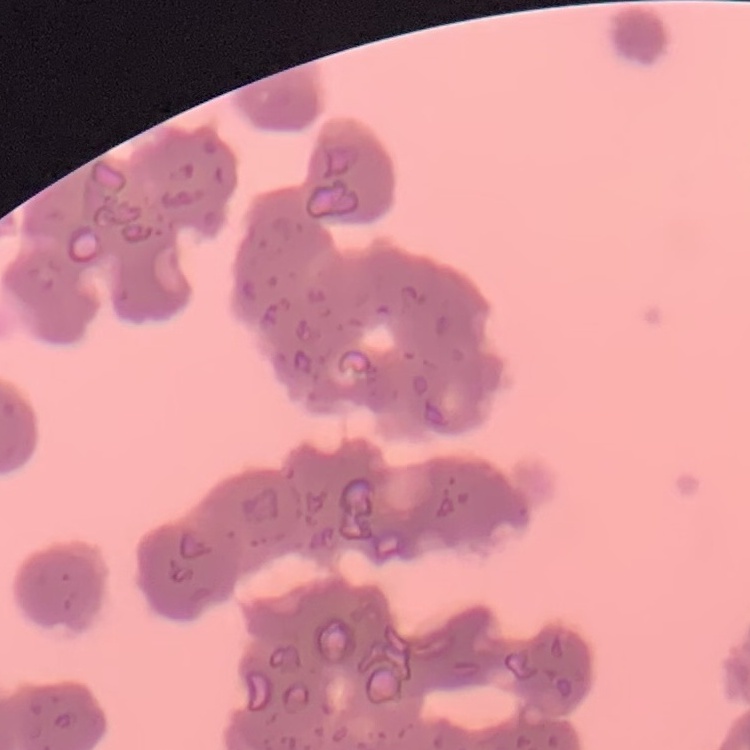
Summary:
  - Erythrocyte morphology: rouleaux formation
  - Stain: Field's or Giemsa
  - Preparation: thin peripheral smear
  - Image type: one tile cut from a larger photomicrograph